Comment on the morphology of the erythrocytes.
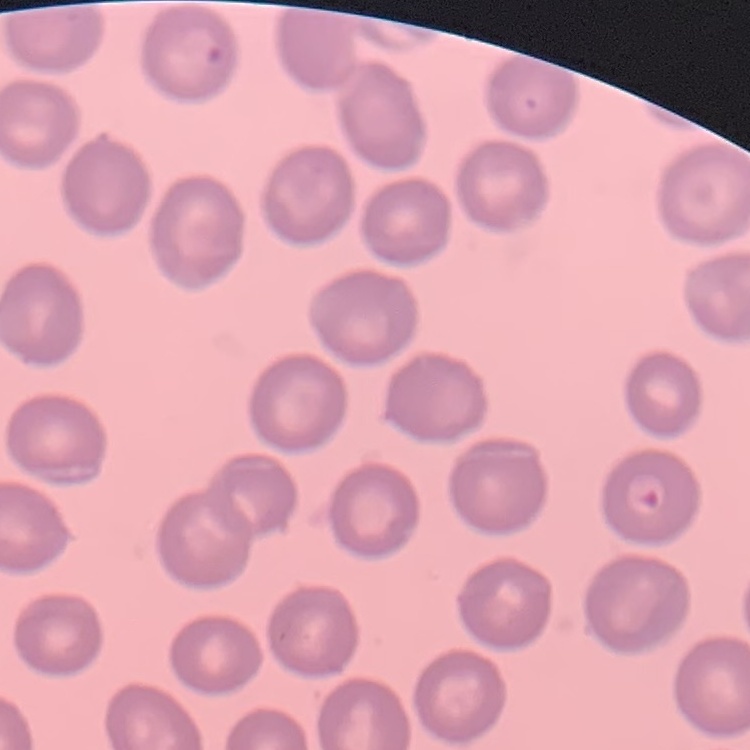
They show no rouleaux formation.

Field's or Giemsa stain. Thin blood smear. Square crop of a larger photomicrograph.